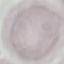

malaria status = uninfected
capture = smartphone through the microscope eyepiece
preparation = thin blood film
stain = Giemsa
image type = automatically extracted cell patch, resized to 64 × 64 pixels